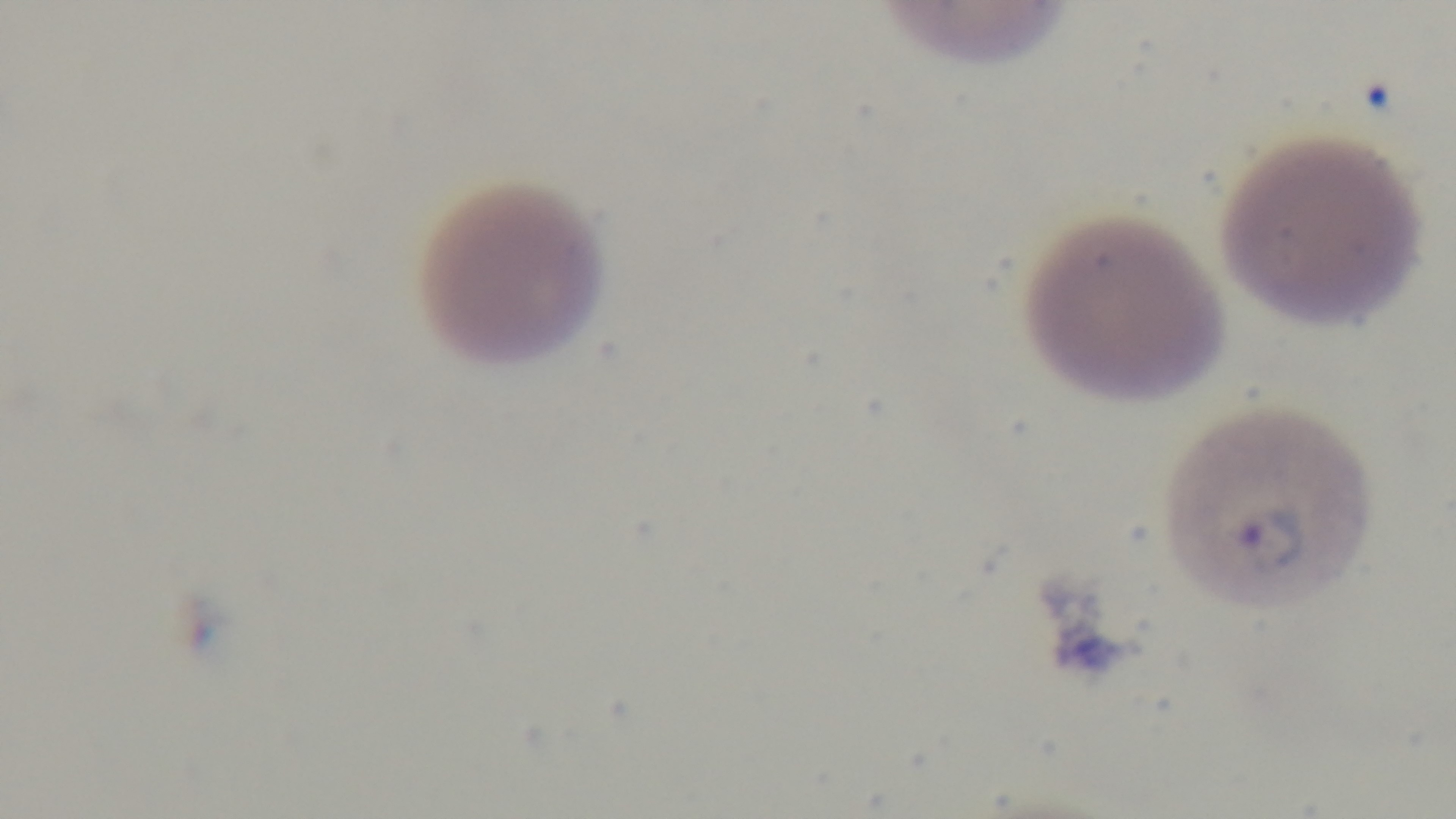
{
  "capture": "mounted 4K digital camera",
  "malaria_status": "infected",
  "stain": "Giemsa",
  "modality": "light microscopy",
  "preparation": "thin",
  "field_of_view": "one from the slide",
  "objective": "100x oil immersion"
}